Point out each Plasmodium parasite.
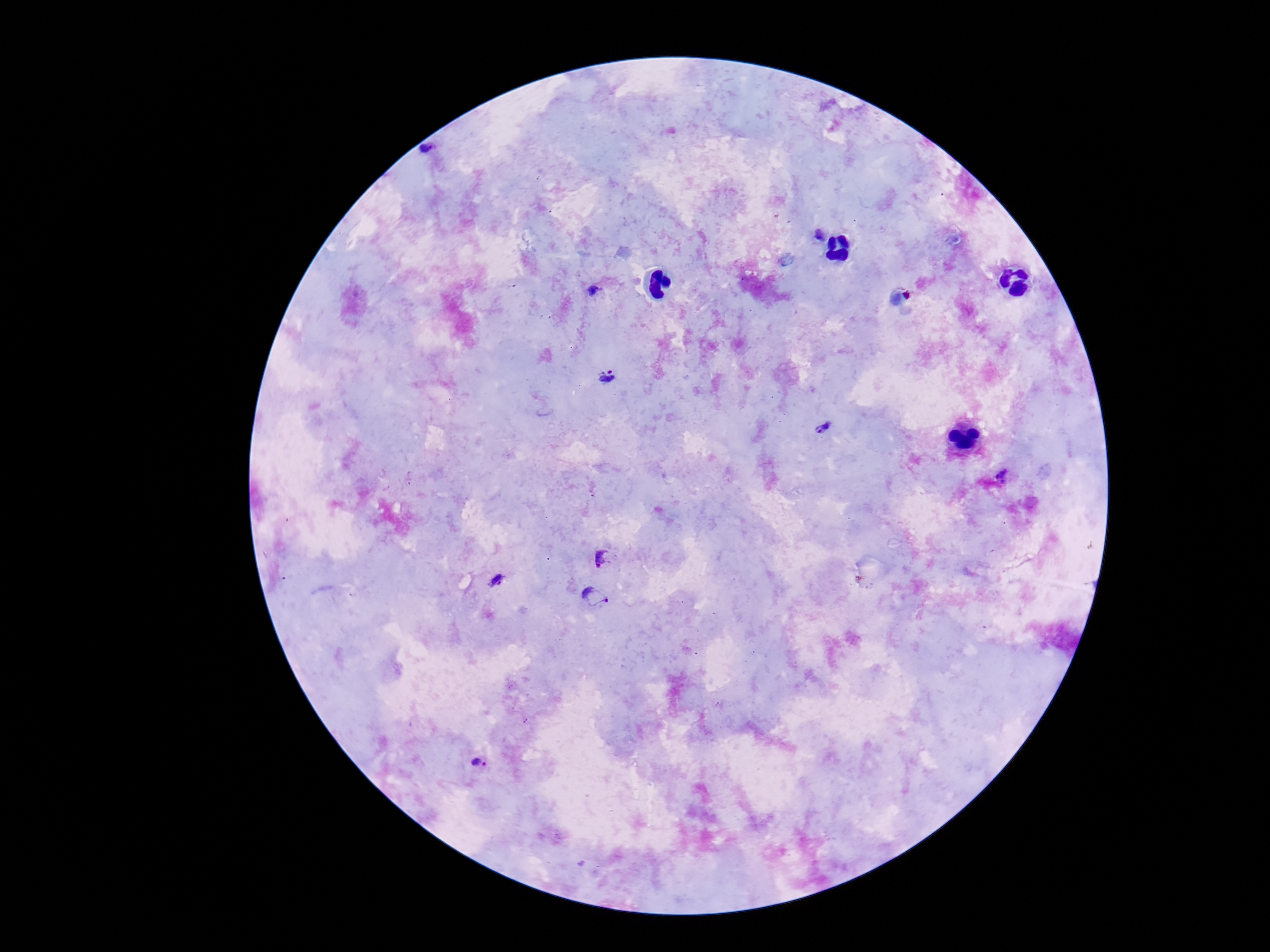
Approximate centers as (x, y) in pixels.
Plasmodium parasites: (427, 149), (820, 235), (593, 292), (611, 380), (823, 427), (1004, 477), (602, 557), (499, 581), (597, 597), (479, 766).

Photographed through the microscope eyepiece with a smartphone camera. Giemsa stain. Patient malaria status: positive. 100x magnification. Thick peripheral-blood smear. Image is 1270×952 pixels. One field from this slide.